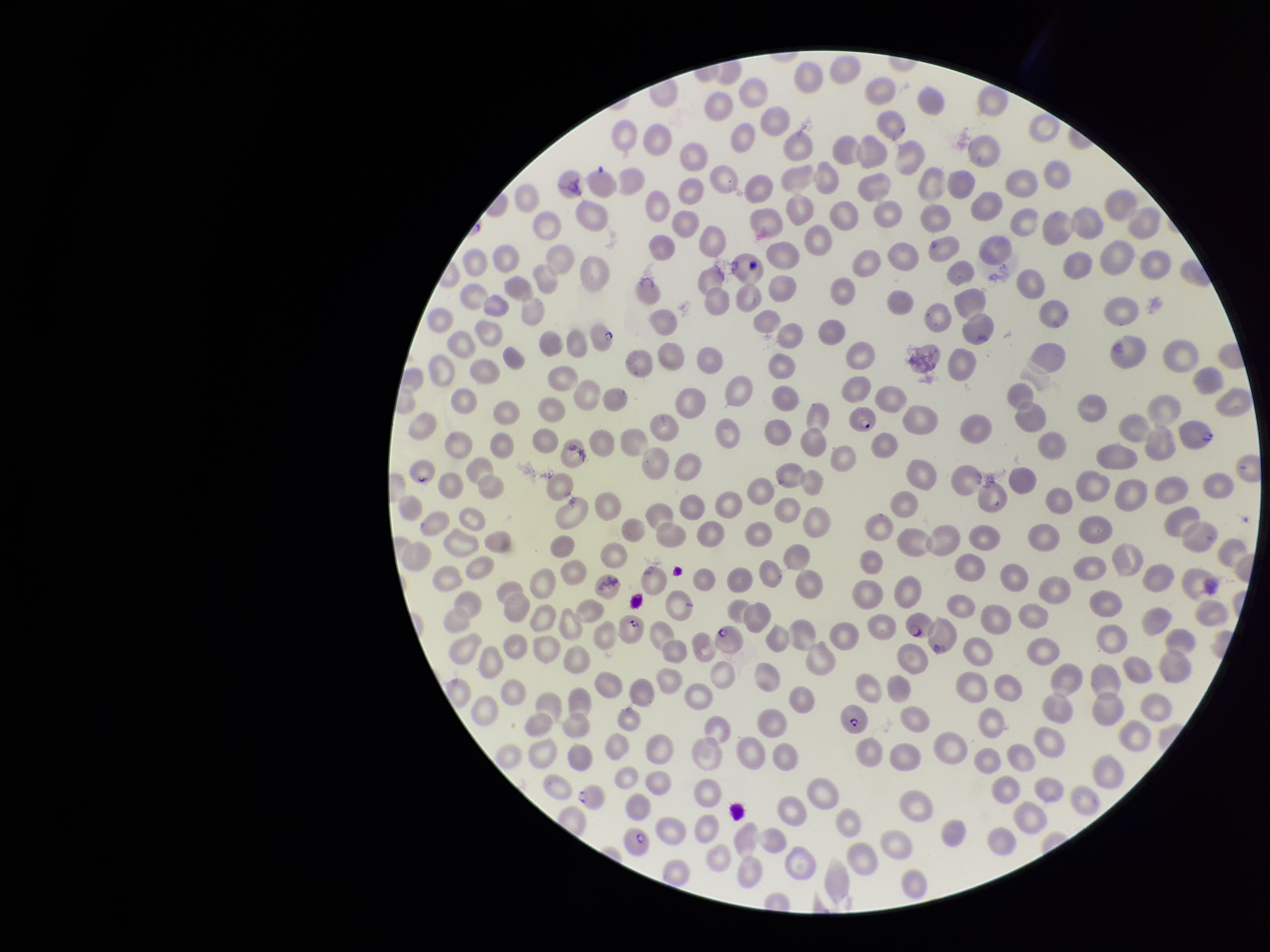

{
  "parasitized_red_blood_cell_count": 10,
  "preparation": "thin blood smear",
  "species_reported_for_this_patient": "Plasmodium falciparum",
  "field_of_view": "one from this slide",
  "stain": "Giemsa",
  "parasitized_red_blood_cells": "detected",
  "red_blood_cell_count": 317,
  "image_size": "1270×952 pixels",
  "capture": "smartphone photograph through the microscope eyepiece",
  "patient_malaria_status": "positive"
}